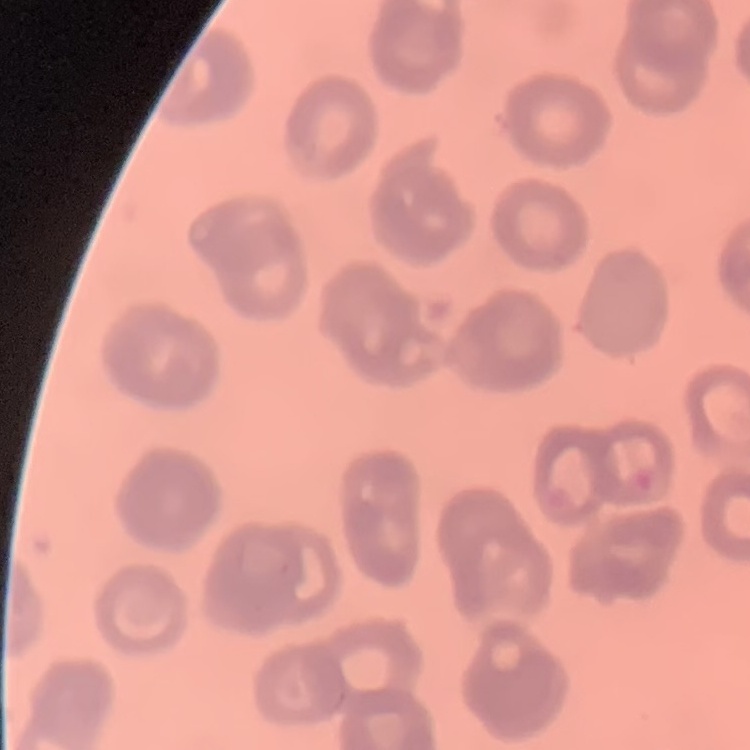

The erythrocytes show rouleaux formation. Thin blood smear. Field's or Giemsa stain. Square crop of a larger photomicrograph.